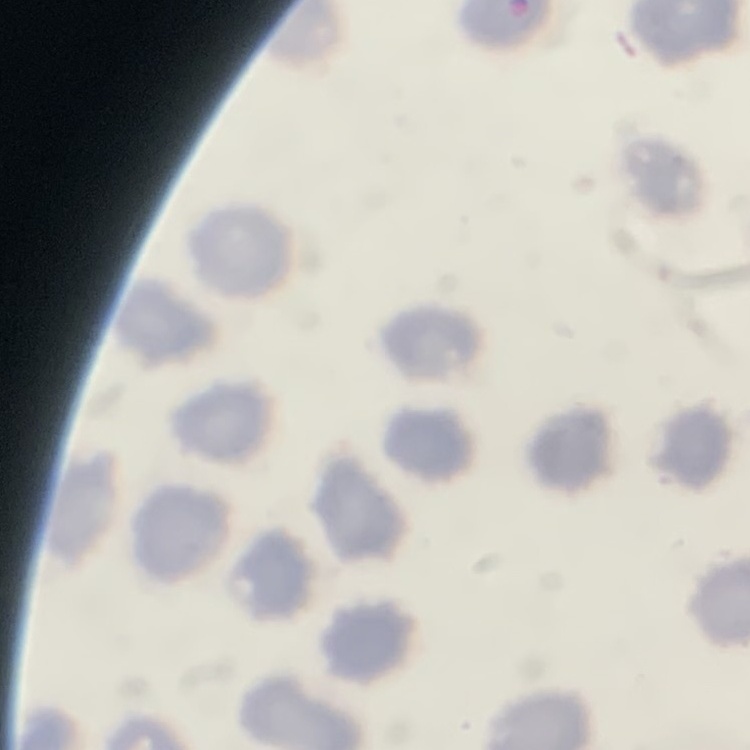
{
  "erythrocyte_morphology": "no rouleaux formation",
  "image_type": "square crop of a larger photomicrograph",
  "stain": "Field's or Giemsa",
  "preparation": "thin peripheral smear"
}